Report the malaria status.
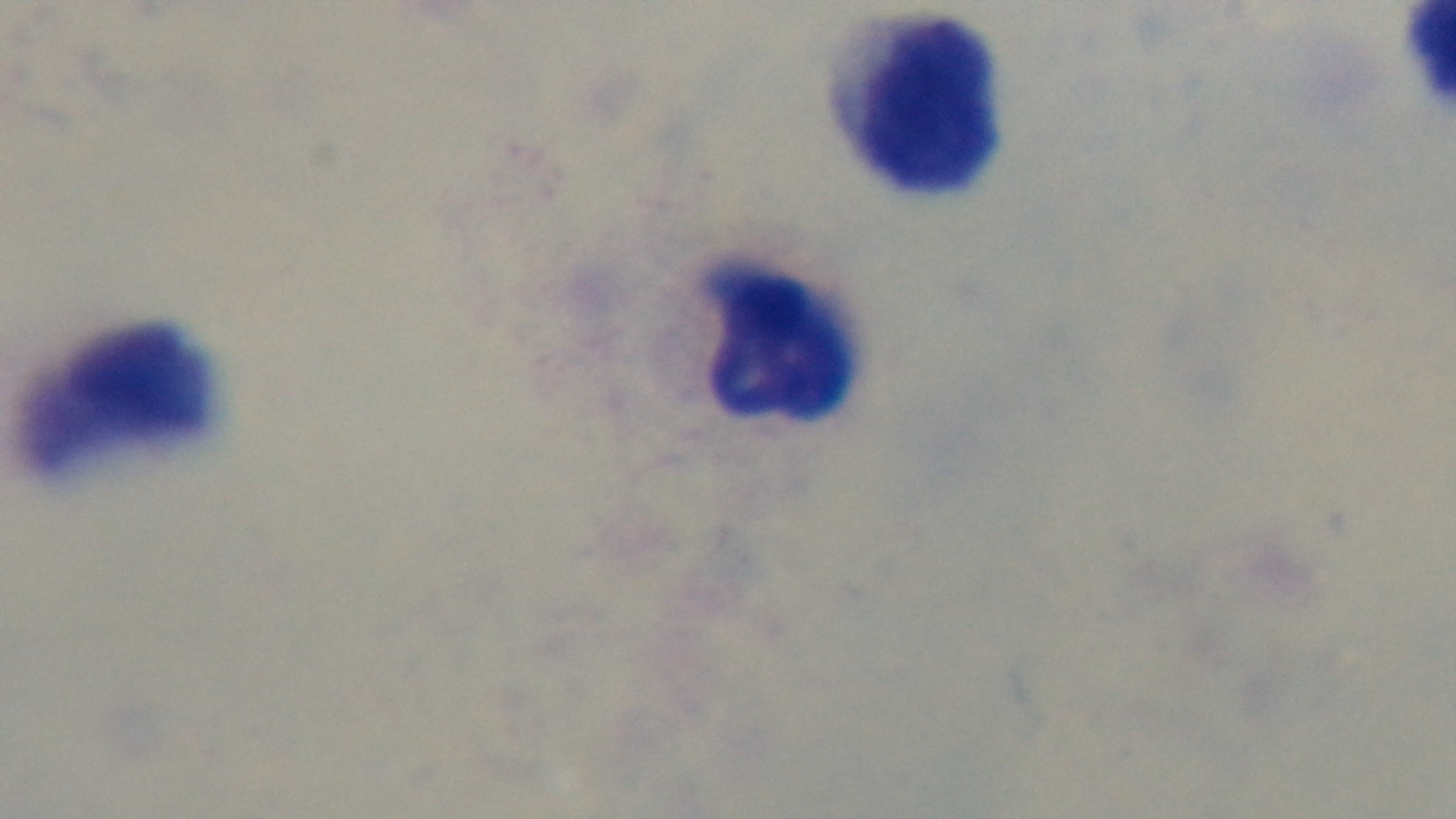
Negative.

objective: 100x oil immersion
modality: light microscopy
field_of_view: one from the slide
capture: mounted 4K digital camera
stain: Giemsa
preparation: thick smear